Report the malaria status of this cell.
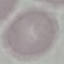

It is uninfected.

capture = smartphone through the microscope eyepiece
stain = Giemsa
image type = automatically extracted cell patch, resized to 64 × 64 pixels
preparation = thin smear